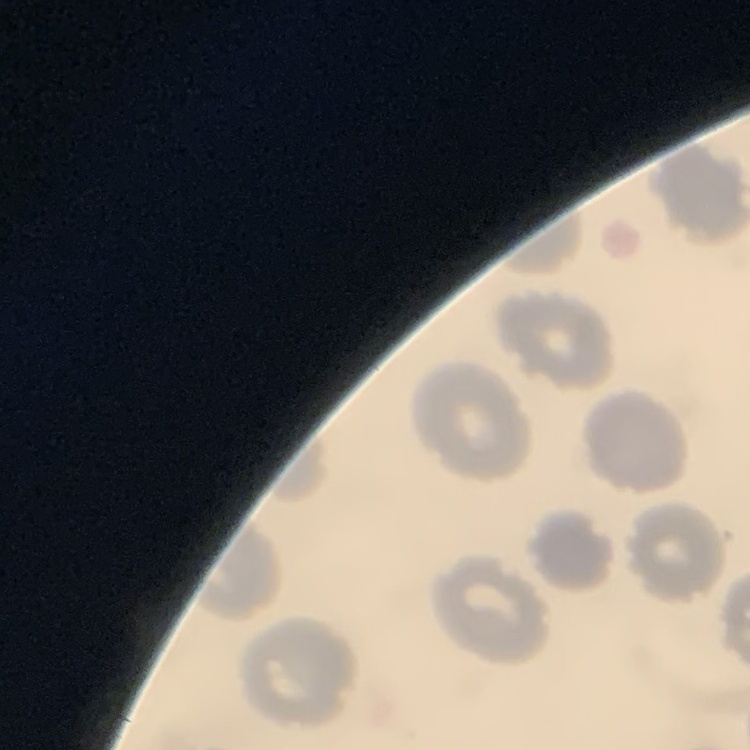

erythrocyte morphology = no rouleaux formation
stain = Field's or Giemsa
preparation = thin blood smear
image type = square crop of a larger photomicrograph